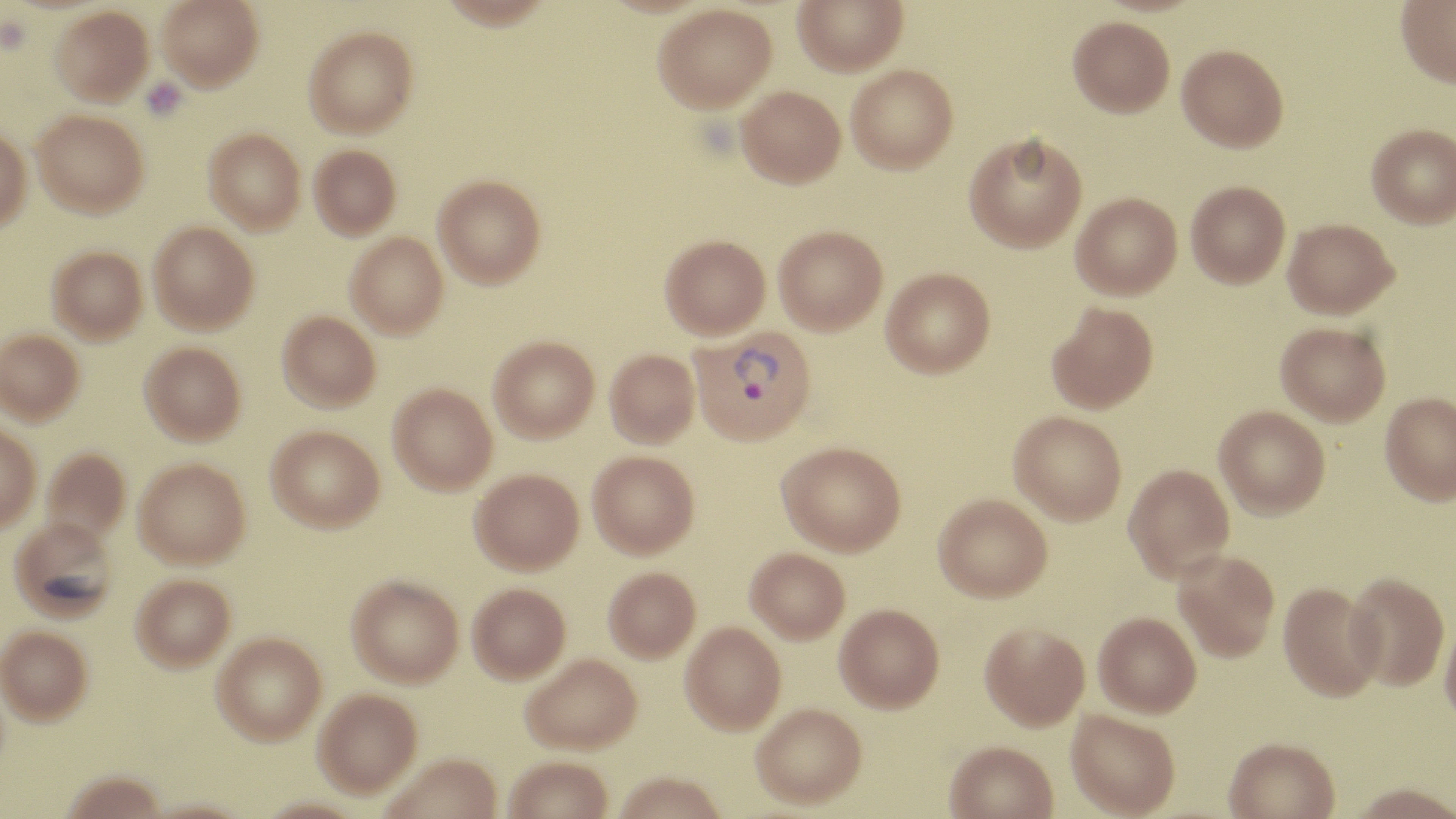

Approximate bounding boxes as named x1/y1/x2/y2 corners in pixels. Platelet locations: (x1=141, y1=78, x2=187, y2=121). Uninfected red blood cell locations: (x1=157, y1=0, x2=263, y2=90), (x1=792, y1=0, x2=907, y2=75), (x1=1396, y1=0, x2=1456, y2=88), (x1=653, y1=3, x2=777, y2=113), (x1=50, y1=6, x2=153, y2=105), (x1=1068, y1=16, x2=1175, y2=117), (x1=304, y1=26, x2=418, y2=137), (x1=1176, y1=44, x2=1289, y2=152), (x1=846, y1=64, x2=958, y2=174), (x1=736, y1=85, x2=845, y2=188), (x1=32, y1=109, x2=149, y2=217), (x1=0, y1=123, x2=32, y2=235), (x1=1366, y1=123, x2=1456, y2=228), (x1=204, y1=128, x2=306, y2=233), (x1=964, y1=131, x2=1087, y2=252), (x1=309, y1=144, x2=401, y2=239), (x1=433, y1=174, x2=545, y2=287), (x1=1186, y1=180, x2=1290, y2=288), (x1=1071, y1=192, x2=1182, y2=299), (x1=1283, y1=218, x2=1398, y2=318), (x1=149, y1=221, x2=258, y2=333), (x1=773, y1=225, x2=887, y2=335), (x1=345, y1=232, x2=449, y2=337), (x1=660, y1=234, x2=770, y2=338), (x1=48, y1=245, x2=147, y2=342), (x1=881, y1=267, x2=995, y2=377), (x1=1046, y1=301, x2=1158, y2=414), (x1=278, y1=310, x2=380, y2=411), (x1=1276, y1=321, x2=1391, y2=426), (x1=0, y1=329, x2=84, y2=424), (x1=489, y1=336, x2=599, y2=441), (x1=139, y1=341, x2=246, y2=444), (x1=604, y1=348, x2=699, y2=447), (x1=388, y1=383, x2=497, y2=494), (x1=1380, y1=392, x2=1456, y2=505), (x1=1214, y1=405, x2=1330, y2=519), (x1=1009, y1=411, x2=1127, y2=524), (x1=0, y1=422, x2=41, y2=531), (x1=266, y1=424, x2=384, y2=531), (x1=777, y1=441, x2=906, y2=555), (x1=41, y1=447, x2=131, y2=543), (x1=588, y1=450, x2=699, y2=557), (x1=134, y1=457, x2=250, y2=567), (x1=1124, y1=463, x2=1235, y2=581), (x1=471, y1=468, x2=584, y2=574), (x1=933, y1=493, x2=1052, y2=602), (x1=9, y1=516, x2=119, y2=621), (x1=745, y1=547, x2=850, y2=643), (x1=1173, y1=551, x2=1280, y2=662), (x1=603, y1=566, x2=701, y2=662), (x1=131, y1=573, x2=235, y2=671), (x1=1344, y1=573, x2=1449, y2=691), (x1=347, y1=574, x2=464, y2=686), (x1=1279, y1=582, x2=1384, y2=702), (x1=467, y1=583, x2=570, y2=683), (x1=835, y1=603, x2=944, y2=712), (x1=1094, y1=612, x2=1201, y2=717), (x1=1440, y1=616, x2=1456, y2=731), (x1=680, y1=621, x2=787, y2=734), (x1=979, y1=621, x2=1090, y2=730), (x1=0, y1=625, x2=92, y2=724), (x1=212, y1=632, x2=326, y2=744), (x1=521, y1=653, x2=642, y2=753), (x1=313, y1=688, x2=422, y2=797), (x1=750, y1=703, x2=867, y2=808), (x1=1066, y1=710, x2=1180, y2=817), (x1=1223, y1=737, x2=1339, y2=819), (x1=944, y1=741, x2=1058, y2=819), (x1=381, y1=752, x2=503, y2=819), (x1=503, y1=755, x2=614, y2=819), (x1=61, y1=770, x2=166, y2=818), (x1=613, y1=771, x2=727, y2=819), (x1=1347, y1=784, x2=1456, y2=819). Plasmodium vivax-infected red blood cell locations: (x1=690, y1=327, x2=816, y2=445). Slide-level diagnosis: Plasmodium vivax. Captured at 1000x magnification. May-Grünwald-Giemsa stain. One field of a larger specimen. Image is 1456×819 pixels. Light microscopy. Thin blood film.